Report the malaria status of this cell.
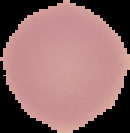

Uninfected.

{
  "image_size": "130×133 pixels",
  "image_type": "cell region segmented out of the field of view; surrounding area masked to black",
  "preparation": "thin blood film"
}